Locate every Plasmodium ovale-infected red blood cell.
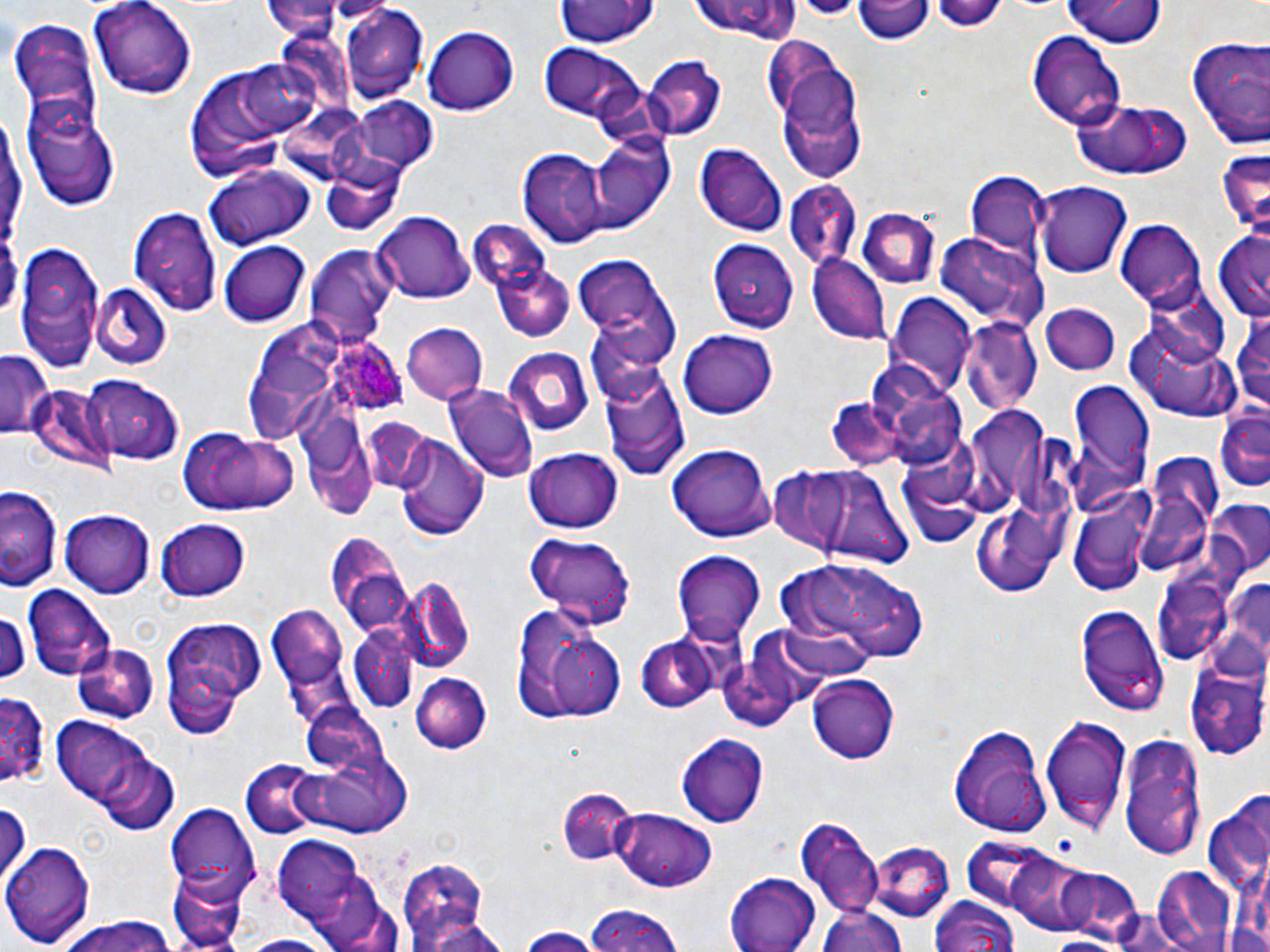
Approximate bounding boxes as named x1/y1/x2/y2 corners in pixels.
Plasmodium ovale-infected red blood cells: (x1=326, y1=333, x2=407, y2=411).

Uninfected red blood cell locations: (x1=89, y1=0, x2=198, y2=100), (x1=553, y1=0, x2=658, y2=49), (x1=689, y1=0, x2=805, y2=44), (x1=854, y1=0, x2=933, y2=45), (x1=265, y1=1, x2=353, y2=38), (x1=1062, y1=1, x2=1164, y2=50), (x1=341, y1=8, x2=429, y2=101), (x1=10, y1=17, x2=100, y2=118), (x1=424, y1=27, x2=519, y2=117), (x1=1027, y1=34, x2=1125, y2=130), (x1=760, y1=37, x2=847, y2=121), (x1=1186, y1=37, x2=1270, y2=146), (x1=537, y1=41, x2=651, y2=133), (x1=766, y1=48, x2=868, y2=182), (x1=243, y1=56, x2=334, y2=133), (x1=644, y1=58, x2=726, y2=143), (x1=21, y1=91, x2=121, y2=211), (x1=350, y1=97, x2=439, y2=173), (x1=1070, y1=98, x2=1192, y2=181), (x1=586, y1=134, x2=673, y2=231), (x1=693, y1=144, x2=786, y2=236), (x1=1215, y1=148, x2=1269, y2=238), (x1=518, y1=151, x2=607, y2=246), (x1=323, y1=160, x2=409, y2=234), (x1=204, y1=164, x2=313, y2=249), (x1=965, y1=172, x2=1048, y2=256), (x1=1034, y1=179, x2=1134, y2=276), (x1=785, y1=183, x2=861, y2=272), (x1=130, y1=205, x2=222, y2=315), (x1=861, y1=207, x2=940, y2=286), (x1=372, y1=211, x2=473, y2=304), (x1=1115, y1=221, x2=1205, y2=309), (x1=1213, y1=228, x2=1270, y2=325), (x1=937, y1=234, x2=1047, y2=331), (x1=15, y1=239, x2=105, y2=369), (x1=480, y1=239, x2=575, y2=344), (x1=708, y1=240, x2=799, y2=327), (x1=218, y1=242, x2=308, y2=326), (x1=303, y1=245, x2=394, y2=349), (x1=574, y1=255, x2=679, y2=364), (x1=808, y1=256, x2=891, y2=343), (x1=91, y1=286, x2=174, y2=370), (x1=886, y1=294, x2=975, y2=399), (x1=1043, y1=304, x2=1121, y2=376), (x1=1229, y1=305, x2=1270, y2=417), (x1=961, y1=320, x2=1043, y2=412), (x1=1129, y1=320, x2=1242, y2=421), (x1=399, y1=322, x2=489, y2=406), (x1=677, y1=330, x2=778, y2=418), (x1=240, y1=344, x2=333, y2=443), (x1=501, y1=347, x2=594, y2=439), (x1=1, y1=350, x2=51, y2=439), (x1=599, y1=364, x2=690, y2=481), (x1=82, y1=373, x2=184, y2=465), (x1=27, y1=384, x2=112, y2=473), (x1=445, y1=384, x2=539, y2=483), (x1=1062, y1=384, x2=1153, y2=510), (x1=892, y1=389, x2=972, y2=471), (x1=826, y1=398, x2=913, y2=463), (x1=973, y1=412, x2=1054, y2=515), (x1=1215, y1=412, x2=1270, y2=495), (x1=362, y1=419, x2=441, y2=494), (x1=175, y1=425, x2=300, y2=516), (x1=306, y1=430, x2=383, y2=520), (x1=393, y1=433, x2=490, y2=543), (x1=669, y1=443, x2=774, y2=538), (x1=522, y1=446, x2=624, y2=533), (x1=1137, y1=450, x2=1222, y2=582), (x1=899, y1=461, x2=982, y2=547), (x1=774, y1=463, x2=845, y2=562), (x1=810, y1=465, x2=914, y2=571), (x1=0, y1=484, x2=62, y2=589), (x1=1211, y1=501, x2=1270, y2=576), (x1=1067, y1=504, x2=1151, y2=597), (x1=61, y1=511, x2=153, y2=598), (x1=976, y1=513, x2=1055, y2=599), (x1=154, y1=518, x2=250, y2=604), (x1=523, y1=532, x2=636, y2=629), (x1=321, y1=534, x2=410, y2=630), (x1=673, y1=551, x2=767, y2=642), (x1=783, y1=558, x2=933, y2=665), (x1=1221, y1=571, x2=1270, y2=668), (x1=400, y1=577, x2=475, y2=673), (x1=1160, y1=582, x2=1232, y2=667), (x1=23, y1=584, x2=116, y2=680), (x1=1075, y1=602, x2=1169, y2=717), (x1=0, y1=603, x2=30, y2=685), (x1=265, y1=604, x2=352, y2=699), (x1=512, y1=605, x2=627, y2=727), (x1=161, y1=618, x2=272, y2=730), (x1=737, y1=627, x2=836, y2=719), (x1=352, y1=631, x2=415, y2=710), (x1=635, y1=635, x2=720, y2=715), (x1=70, y1=642, x2=159, y2=724), (x1=1184, y1=663, x2=1270, y2=762), (x1=411, y1=670, x2=491, y2=751), (x1=808, y1=672, x2=900, y2=764), (x1=0, y1=690, x2=49, y2=791), (x1=301, y1=708, x2=401, y2=794), (x1=1041, y1=714, x2=1132, y2=833), (x1=49, y1=715, x2=176, y2=827), (x1=948, y1=726, x2=1052, y2=836), (x1=679, y1=733, x2=769, y2=828), (x1=1120, y1=734, x2=1206, y2=862), (x1=294, y1=753, x2=412, y2=837), (x1=240, y1=763, x2=334, y2=841), (x1=555, y1=786, x2=638, y2=865), (x1=0, y1=802, x2=29, y2=888), (x1=167, y1=806, x2=260, y2=894), (x1=614, y1=808, x2=718, y2=891), (x1=1206, y1=809, x2=1268, y2=895), (x1=792, y1=817, x2=885, y2=914), (x1=270, y1=830, x2=394, y2=951), (x1=961, y1=838, x2=1061, y2=917), (x1=2, y1=840, x2=92, y2=946), (x1=871, y1=840, x2=954, y2=919), (x1=1001, y1=853, x2=1114, y2=942), (x1=395, y1=858, x2=492, y2=950), (x1=1056, y1=865, x2=1144, y2=945), (x1=1149, y1=867, x2=1239, y2=952), (x1=723, y1=868, x2=821, y2=951), (x1=167, y1=870, x2=250, y2=952), (x1=928, y1=895, x2=1019, y2=952), (x1=816, y1=905, x2=910, y2=952), (x1=582, y1=906, x2=688, y2=952), (x1=54, y1=917, x2=182, y2=952), (x1=419, y1=919, x2=516, y2=952), (x1=517, y1=926, x2=595, y2=952), (x1=231, y1=933, x2=341, y2=952), (x1=1038, y1=933, x2=1122, y2=951). Slide-level diagnosis: Plasmodium ovale. May-Grünwald-Giemsa-stained preparation. Image is 1270×952 pixels. Single field of view. Thin blood film. 1000x magnification. Light microscopy.